Locate every Plasmodium parasite.
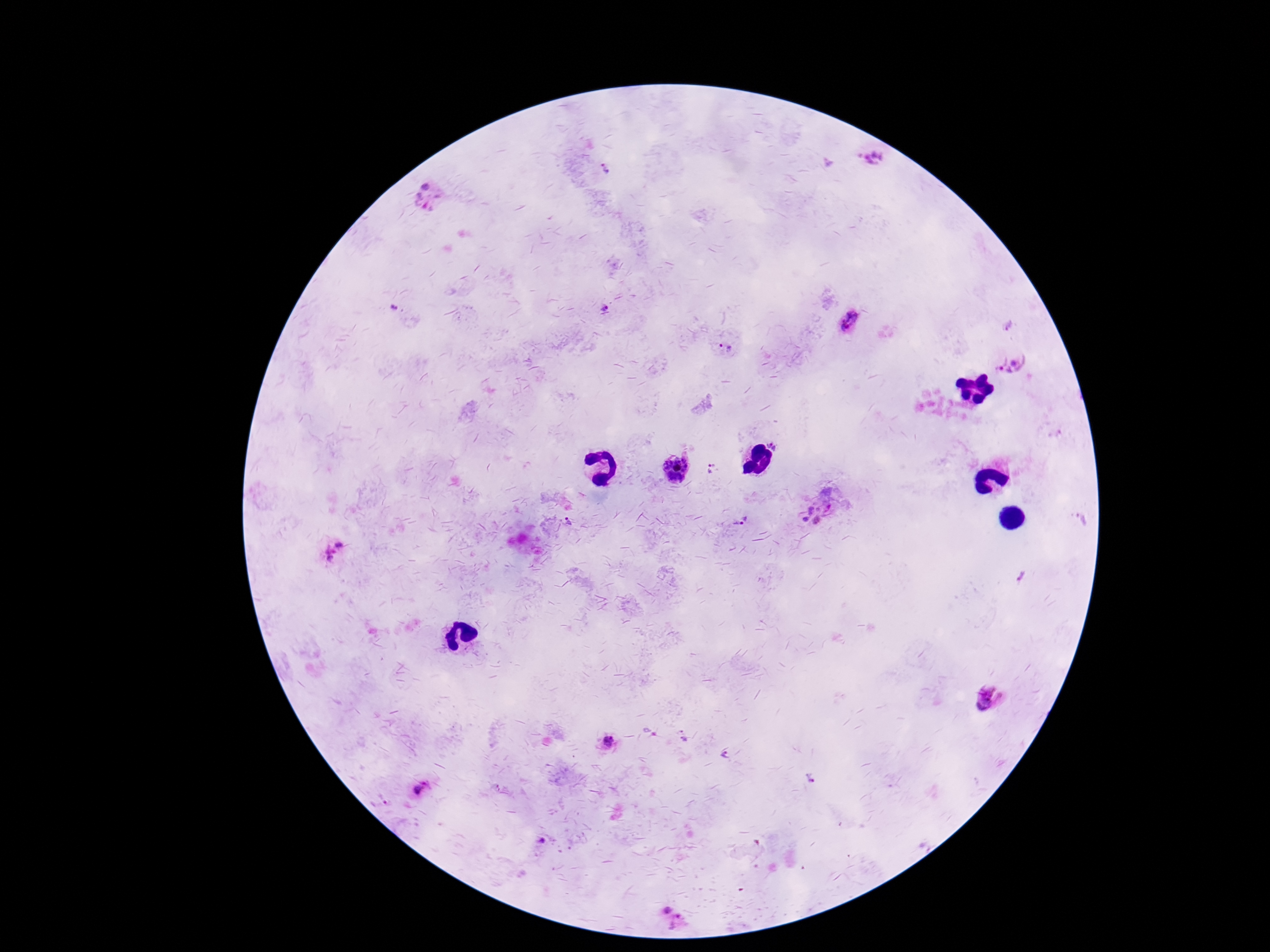
Approximate centers as [x, y] in pixels.
Plasmodium parasites: [873, 157], [606, 170], [430, 198], [394, 307], [604, 307], [850, 321], [1008, 327], [726, 348], [1011, 363], [1056, 433], [773, 445], [677, 468], [711, 468], [828, 497], [811, 510], [806, 519], [1080, 519], [741, 520], [816, 520], [568, 521], [334, 549], [1021, 575], [991, 699], [683, 734], [609, 741], [725, 753], [812, 777], [496, 788], [418, 790], [387, 802], [541, 842], [667, 911], [678, 923].

Summary:
  - Image size: 1270×952 pixels
  - Patient malaria status: positive
  - Preparation: thick peripheral-blood smear
  - Magnification: 100x
  - Capture: smartphone camera through the microscope eyepiece
  - Field of view: one from this slide
  - Stain: Giemsa